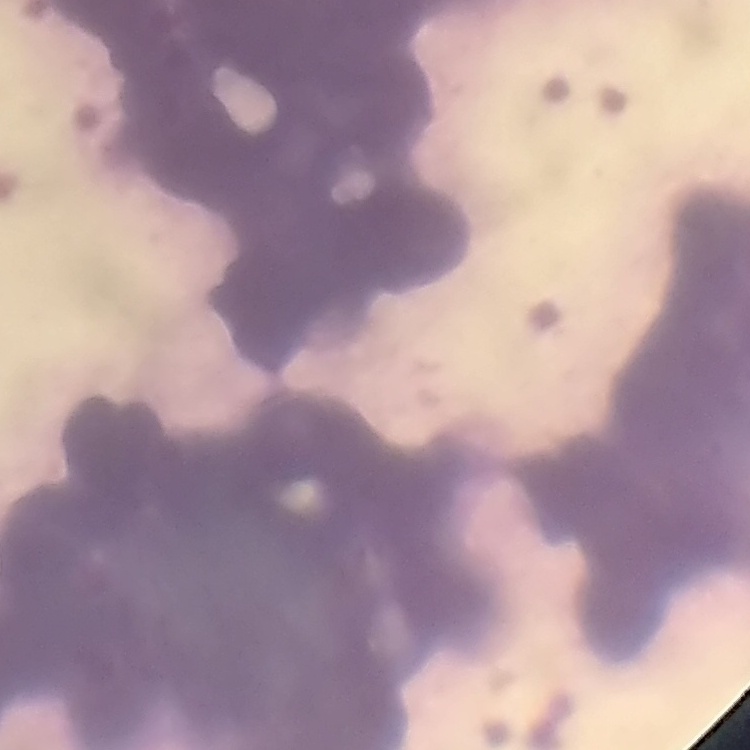

The erythrocytes exhibit rouleaux formation. Thin blood film. Field's or Giemsa stain. One tile cut from a larger photomicrograph.